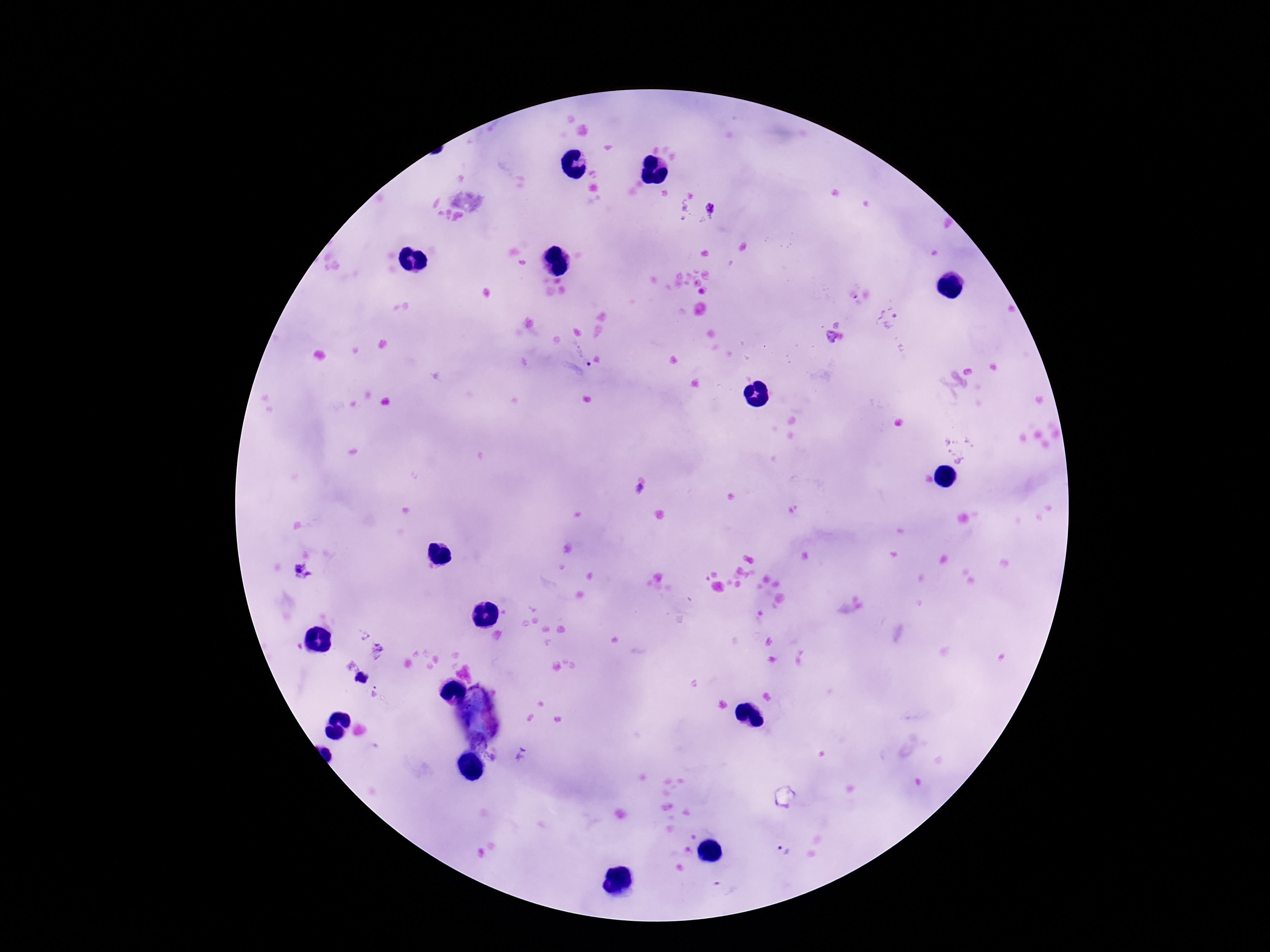

Approximate centers as {x, y} in pixels. Plasmodium parasite locations: {715, 208}, {889, 319}, {833, 338}, {583, 354}, {638, 489}, {302, 572}, {381, 651}, {351, 664}, {373, 693}, {522, 755}, {782, 850}. One field from this slide. Thick blood film. Giemsa stain. Photographed through the microscope eyepiece with a smartphone camera. Patient malaria status: infected. 100x magnification. Image is 1270×952 pixels.